Name the cell type shown.
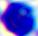

This is a leukocyte.

Photomicrograph. 400x magnification.